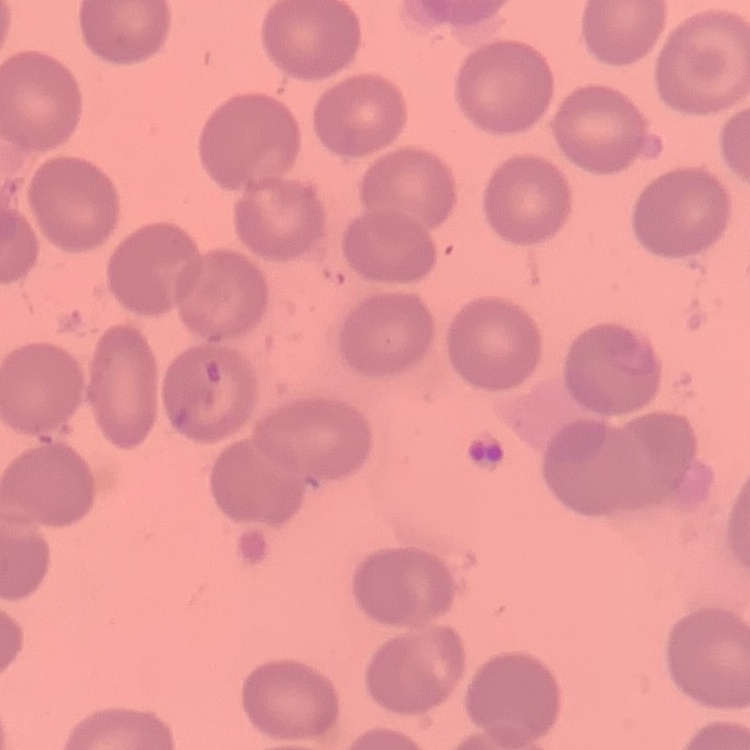 The red blood cells exhibit no rouleaux formation. Thin blood smear. One tile cut from a larger photomicrograph. Stained with either Field's or Giemsa.